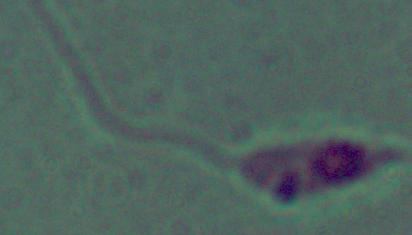

Captured at 1000x magnification. Micrograph. A Leishmania parasite is shown.